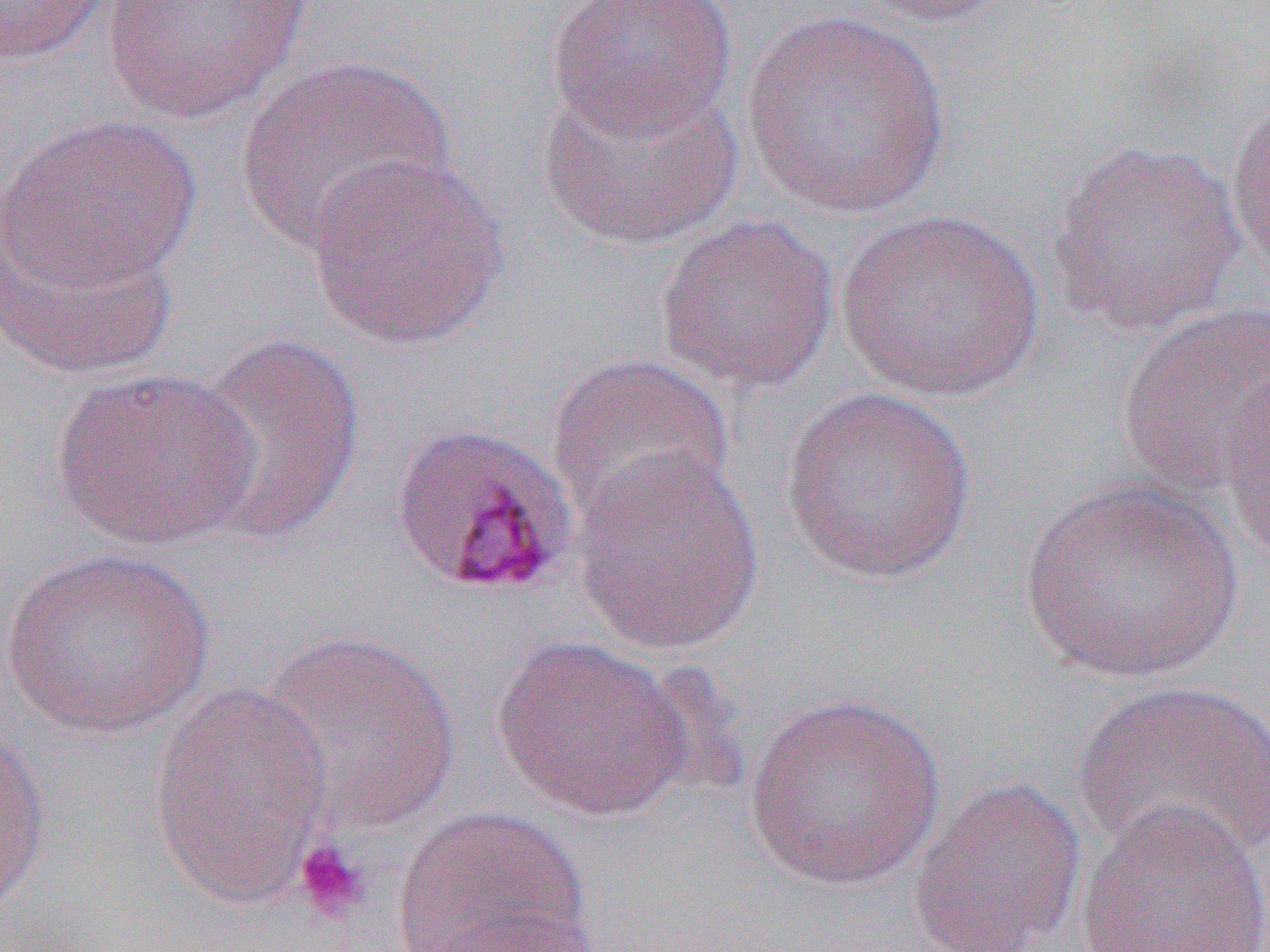
Approximate bounding boxes as named x1/y1/x2/y2 corners in pixels. Uninfected red blood cell locations: (x1=0, y1=0, x2=111, y2=66), (x1=100, y1=0, x2=314, y2=124), (x1=545, y1=0, x2=738, y2=143), (x1=846, y1=0, x2=1019, y2=29), (x1=740, y1=7, x2=952, y2=220), (x1=234, y1=52, x2=456, y2=253), (x1=537, y1=73, x2=745, y2=251), (x1=1225, y1=94, x2=1270, y2=284), (x1=1, y1=113, x2=203, y2=294), (x1=1045, y1=137, x2=1247, y2=336), (x1=305, y1=150, x2=511, y2=352), (x1=833, y1=208, x2=1048, y2=404), (x1=654, y1=211, x2=841, y2=395), (x1=1, y1=213, x2=180, y2=382), (x1=1113, y1=300, x2=1270, y2=503), (x1=186, y1=332, x2=366, y2=546), (x1=547, y1=352, x2=737, y2=529), (x1=48, y1=366, x2=260, y2=551), (x1=1220, y1=371, x2=1269, y2=565), (x1=779, y1=387, x2=979, y2=585), (x1=569, y1=442, x2=768, y2=655), (x1=1016, y1=478, x2=1245, y2=686), (x1=1, y1=546, x2=215, y2=739), (x1=255, y1=628, x2=463, y2=835), (x1=491, y1=634, x2=700, y2=822), (x1=1073, y1=678, x2=1270, y2=869), (x1=146, y1=679, x2=337, y2=912), (x1=744, y1=691, x2=947, y2=891), (x1=0, y1=722, x2=52, y2=920), (x1=906, y1=778, x2=1087, y2=952), (x1=1075, y1=798, x2=1270, y2=952), (x1=390, y1=805, x2=590, y2=951), (x1=426, y1=908, x2=607, y2=951). Platelet locations: (x1=293, y1=836, x2=373, y2=923). Slide-level diagnosis: Plasmodium malariae. Thin blood film. Light microscopy. Single field of view. Captured at 1000x magnification. Image is 1270×952 pixels.